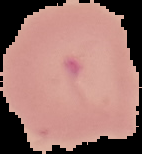
Result: malaria parasites detected. Image is 142×154 pixels. From a thin blood smear. Cell region segmented out of the field of view; the surrounding area is masked to black.